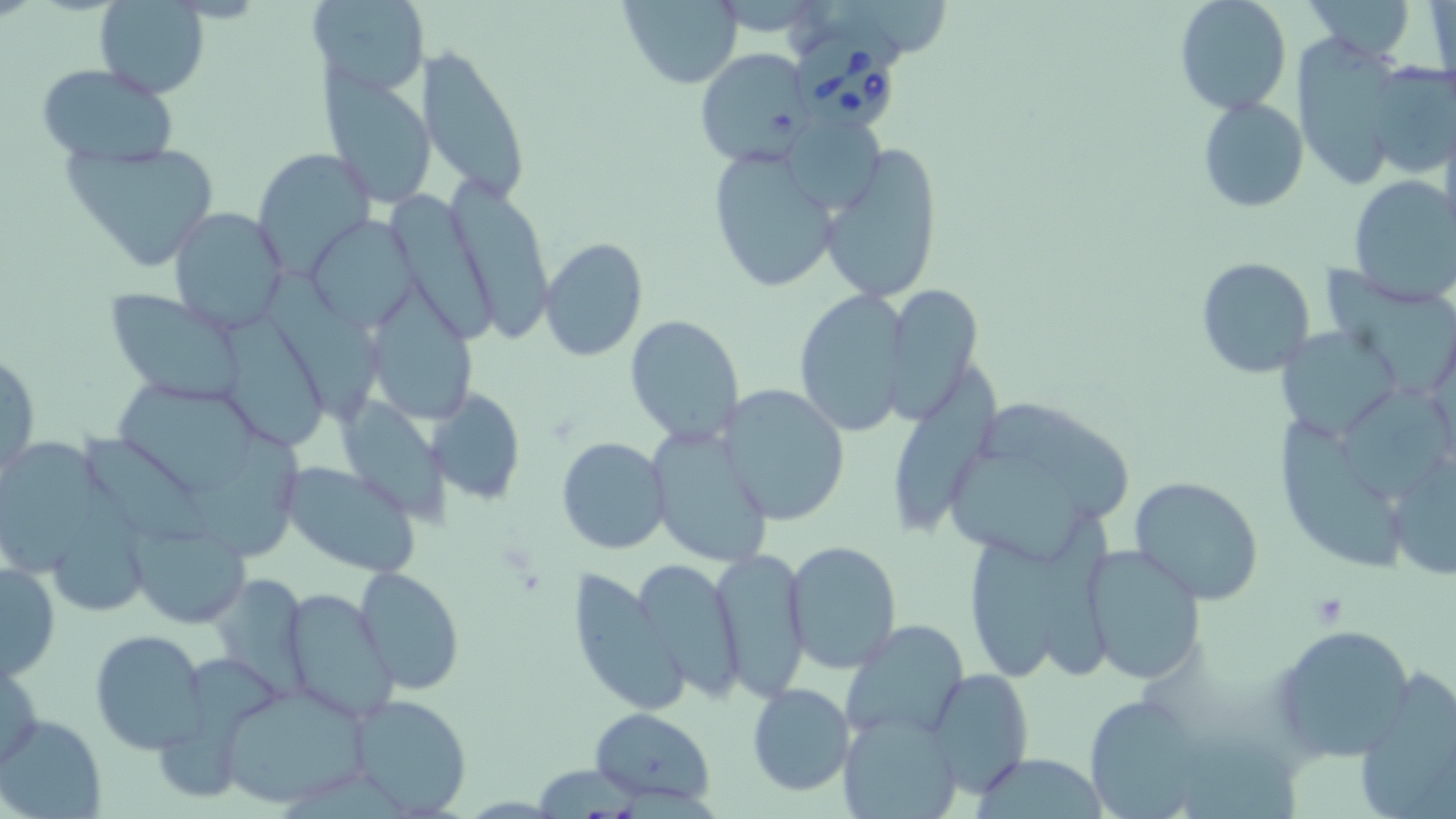

slide-level diagnosis = Babesia divergens
field of view = single
platelet locations = approximate bounding boxes as (x1, y1, x2, y2) in pixels: (1306, 592, 1350, 625)
modality = optical microscopy
Babesia divergens-infected red blood cell locations = approximate bounding boxes as (x1, y1, x2, y2) in pixels: (796, 33, 903, 129)
magnification = 1000x
preparation = thin blood smear
uninfected red blood cell locations = approximate bounding boxes as (x1, y1, x2, y2) in pixels: (310, 0, 429, 95), (1173, 0, 1292, 115), (1299, 0, 1419, 64), (93, 1, 211, 99), (613, 1, 744, 87), (1426, 1, 1455, 95), (1292, 34, 1404, 190), (420, 45, 533, 200), (695, 48, 810, 168), (1364, 59, 1456, 179), (35, 63, 179, 166), (320, 70, 437, 206), (1197, 96, 1309, 213), (788, 120, 893, 213), (63, 139, 221, 272), (821, 143, 945, 304), (706, 144, 845, 294), (253, 148, 376, 275), (449, 174, 557, 341), (1347, 176, 1456, 303), (388, 188, 504, 347), (168, 206, 289, 334), (306, 215, 420, 332), (539, 237, 648, 361), (1196, 256, 1316, 378), (1318, 258, 1456, 397), (269, 267, 385, 416), (884, 281, 981, 425), (371, 284, 478, 417), (795, 288, 912, 434), (106, 289, 247, 406), (222, 311, 332, 444), (625, 313, 745, 445), (1277, 322, 1403, 443), (1, 348, 40, 480), (896, 362, 1007, 523), (105, 378, 262, 494), (1337, 380, 1456, 508), (718, 384, 853, 525), (428, 387, 527, 507), (982, 393, 1138, 519), (338, 397, 448, 521), (1279, 419, 1403, 573), (646, 424, 775, 570), (84, 427, 221, 544), (183, 428, 306, 556), (0, 435, 103, 588), (557, 436, 670, 555), (945, 442, 1094, 560), (1385, 447, 1456, 581), (280, 460, 421, 578), (1128, 476, 1265, 604), (65, 485, 150, 611), (1038, 511, 1120, 683), (132, 522, 247, 627), (968, 531, 1072, 683), (785, 541, 901, 672), (1080, 543, 1206, 685), (709, 546, 810, 698), (629, 558, 748, 699), (1, 559, 61, 680), (212, 565, 322, 702), (354, 565, 464, 696), (566, 565, 689, 718), (282, 588, 396, 724), (840, 620, 968, 739), (1270, 624, 1419, 763), (90, 629, 208, 754), (1, 651, 45, 771), (157, 655, 285, 803), (925, 668, 1034, 797), (1354, 671, 1456, 819), (216, 683, 375, 808), (747, 684, 855, 796), (348, 693, 471, 816), (1083, 694, 1209, 818), (588, 707, 716, 809), (839, 711, 964, 819), (0, 713, 105, 819), (1185, 732, 1304, 819), (973, 751, 1107, 818)
image size = 1456×819 pixels
stain = May-Grünwald-Giemsa